Identify the parasite.
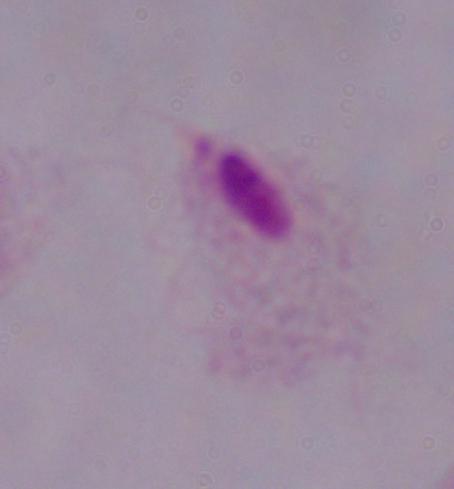

A trichomonad.

Captured at 1000x magnification. Photomicrograph.